Comment on the background quality.
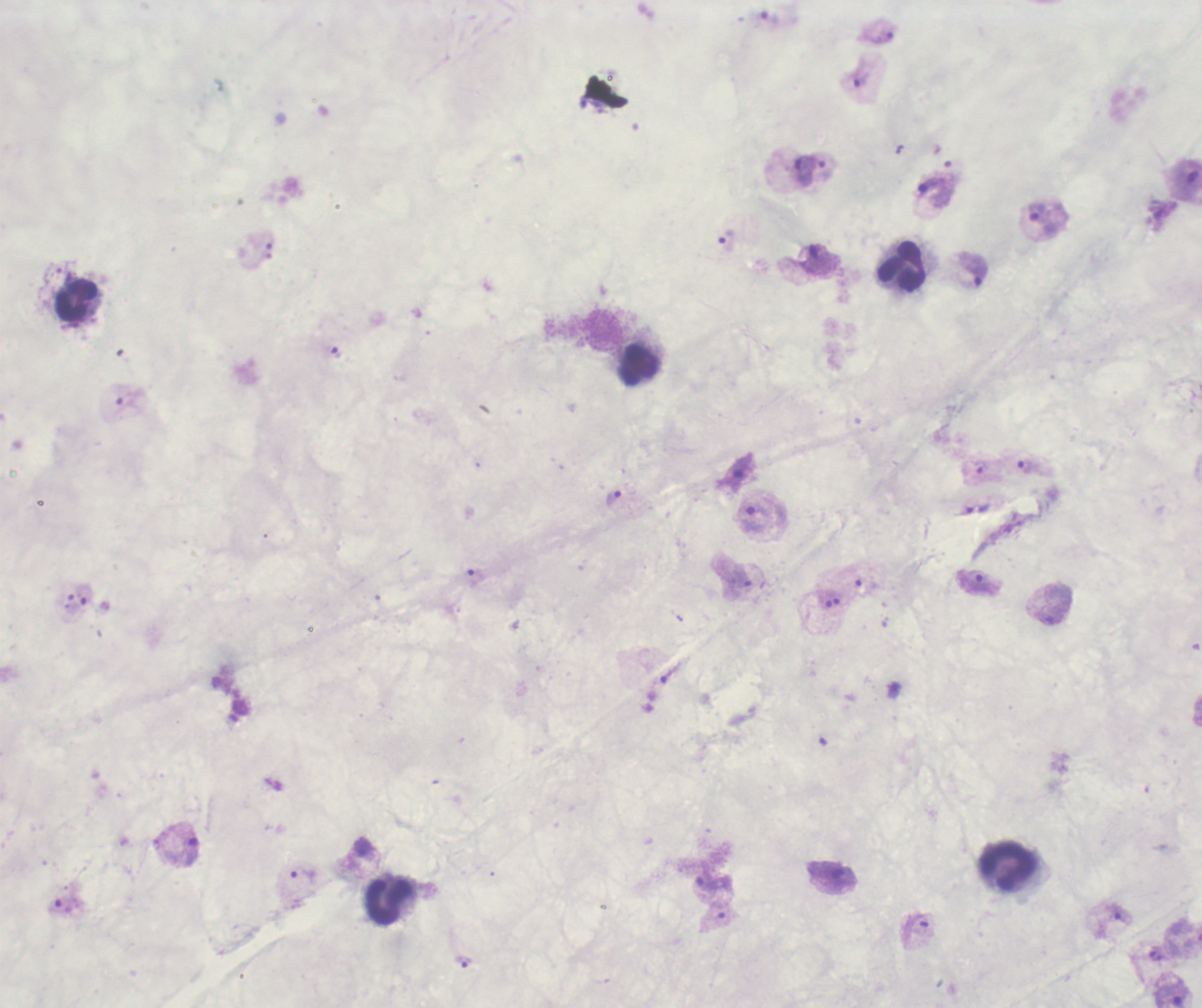
It is poor.

stain: Romanowsky
magnification: 100x
result: Plasmodium parasites identified
image_size: 1202×1008 pixels
preparation: thick smear of blood
trophozoite_locations: 'approximate centers as (x, y) in pixels: (768, 17), (877, 33), (860, 78), (809, 170), (933, 193), (1042, 219), (726, 239), (973, 270), (335, 352), (1029, 466), (981, 467), (737, 475), (613, 498), (752, 518), (474, 577), (740, 579), (976, 582), (84, 594), (184, 847), (302, 875), (705, 883), (1119, 915), (463, 961)'
leukocyte_locations: 'approximate centers as (x, y) in pixels: (903, 267), (76, 300), (639, 365), (1005, 866), (389, 902)'
field_of_view: one from this slide
context: previously used in an actual diagnosis